Evaluate for malaria.
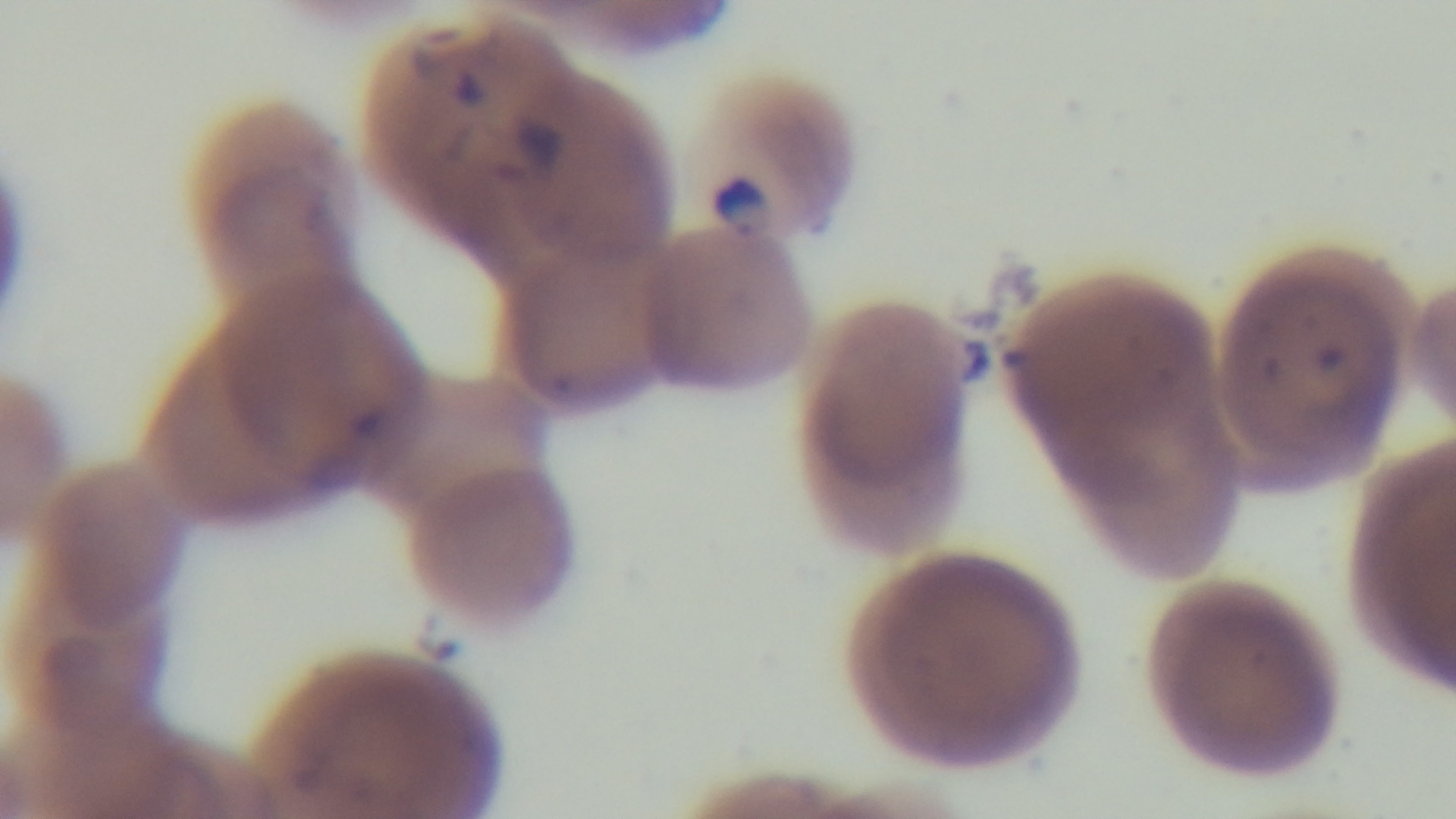

Positive.

Giemsa-stained. Photomicrograph. One field from the slide. Mounted 4K digital camera. Preparation: thin. Oil-immersion objective, 100x.